Name the cell type shown.
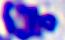

This is a leukocyte.

magnification: 400x
modality: micrograph